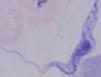 Photomicrograph. A trypanosome is seen. 1000x magnification.